Point out Plasmodium parasites and leukocytes.
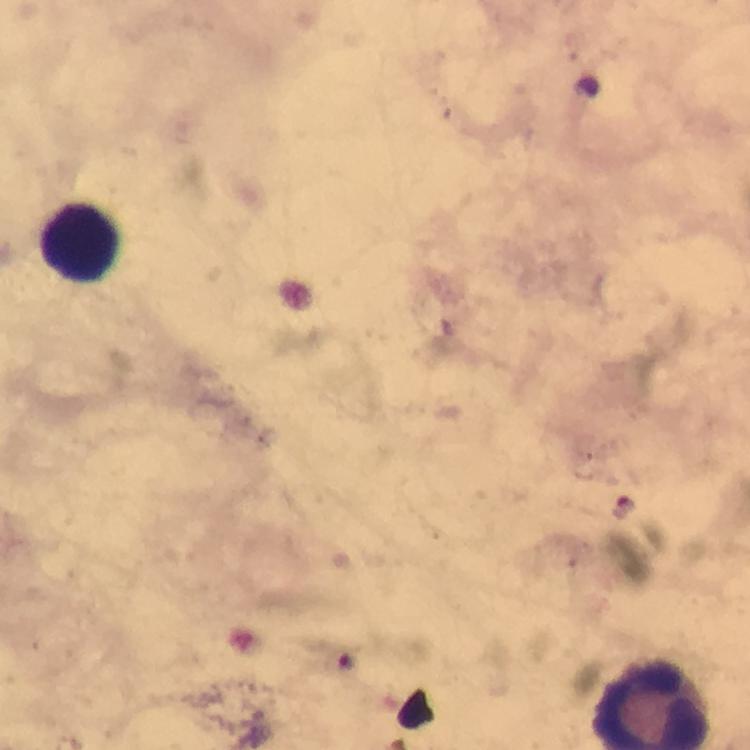
Approximate centers as {x, y} in pixels.
Plasmodium parasites: {625, 506}, {347, 658}.
Leukocytes: {81, 242}.

stain = Giemsa
capture = smartphone camera through the microscope
preparation = thick blood film
magnification = 100x
context = from a malaria diagnostic workup
image size = 750×750 pixels
cropped from = one field of view
immersion oil = used